Locate every uninfected red blood cell.
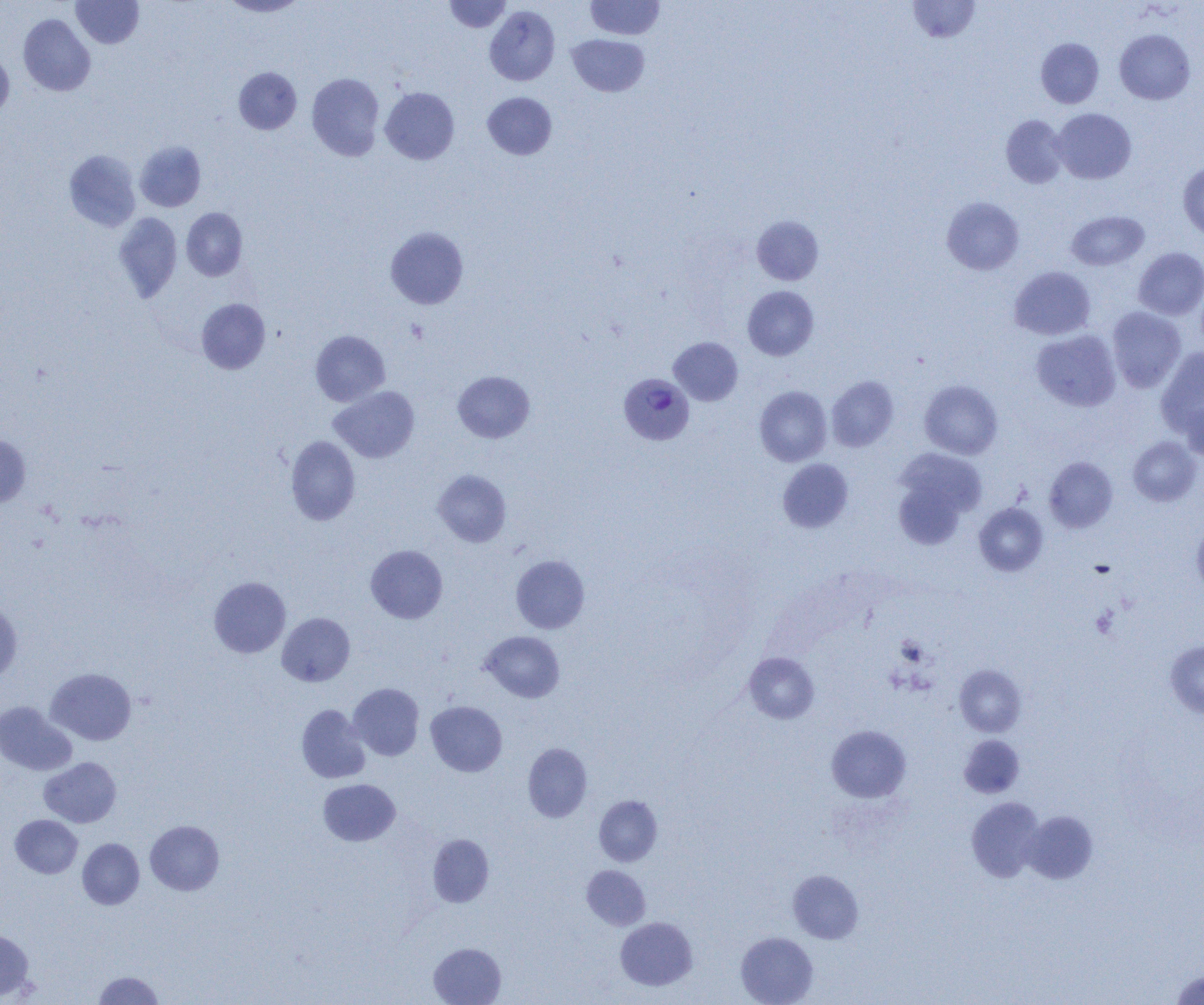

Approximate bounding boxes as (x1, y1, x2, y2) in pixels.
Uninfected red blood cells: (71, 0, 144, 48), (219, 0, 307, 17), (444, 0, 512, 32), (585, 1, 665, 40), (907, 1, 980, 43), (484, 5, 560, 86), (18, 14, 95, 96), (1115, 29, 1195, 104), (567, 33, 650, 97), (1036, 38, 1103, 108), (0, 48, 14, 120), (234, 66, 302, 134), (307, 73, 385, 160), (380, 87, 459, 164), (482, 92, 557, 160), (1052, 108, 1136, 183), (1001, 115, 1068, 188), (135, 141, 206, 212), (63, 150, 141, 232), (1178, 160, 1204, 239), (942, 197, 1024, 274), (181, 208, 248, 281), (1066, 211, 1149, 270), (113, 213, 182, 302), (751, 215, 824, 285), (385, 226, 468, 309), (1133, 247, 1204, 320), (1010, 266, 1095, 340), (743, 286, 819, 360), (196, 298, 270, 374), (1106, 307, 1186, 393), (1032, 329, 1121, 411), (310, 330, 390, 406), (669, 337, 743, 406), (1156, 346, 1204, 438), (453, 370, 535, 443), (826, 376, 899, 452), (919, 380, 1003, 459), (330, 385, 420, 462), (754, 386, 832, 466), (1181, 397, 1204, 460), (0, 434, 31, 506), (286, 435, 360, 525), (1128, 437, 1201, 506), (892, 448, 987, 540), (1045, 456, 1118, 533), (777, 458, 853, 533), (433, 470, 511, 547), (974, 502, 1048, 576), (1192, 522, 1204, 598), (365, 545, 448, 623), (510, 555, 590, 633), (209, 576, 291, 658), (0, 599, 22, 684), (277, 612, 355, 686), (480, 631, 565, 702), (1165, 640, 1204, 718), (743, 652, 819, 724), (955, 665, 1026, 736), (46, 667, 136, 745), (348, 683, 424, 761), (0, 701, 77, 775), (426, 701, 507, 776), (296, 705, 370, 783), (826, 725, 911, 802), (958, 735, 1025, 798), (522, 743, 592, 822), (39, 757, 121, 827), (318, 779, 400, 846), (594, 795, 662, 866), (966, 797, 1044, 882), (1023, 810, 1098, 884), (10, 814, 82, 878), (145, 820, 224, 895), (428, 834, 494, 907), (77, 838, 145, 909), (582, 865, 650, 930), (787, 869, 863, 944), (615, 917, 697, 990), (0, 930, 34, 1001), (735, 932, 818, 1005), (428, 943, 506, 1005), (1169, 969, 1204, 1005), (93, 971, 164, 1004).

Platelet locations: (1091, 607, 1118, 638). Plasmodium vivax-infected red blood cell locations: (619, 373, 695, 445). Slide-level diagnosis: Plasmodium vivax. Single field of view. 1000x magnification. Image is 1204×1005 pixels. Thin blood smear. Light microscopy.